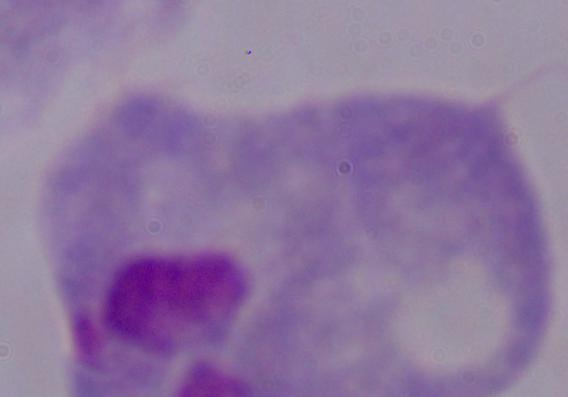
Summary:
  - Modality: micrograph
  - Identification: trichomonad
  - Magnification: 1000x